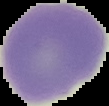 Malaria status: uninfected. Image is 109×106 pixels. The area outside the segmented cell region is set to black. From a thin blood smear.